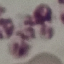
Malaria status: uninfected. Photographed with a smartphone camera at the microscope eyepiece. Thin blood smear. Giemsa stain. Automatically extracted cell patch, resized to 64 × 64 pixels.